Identify the blood parasite species.
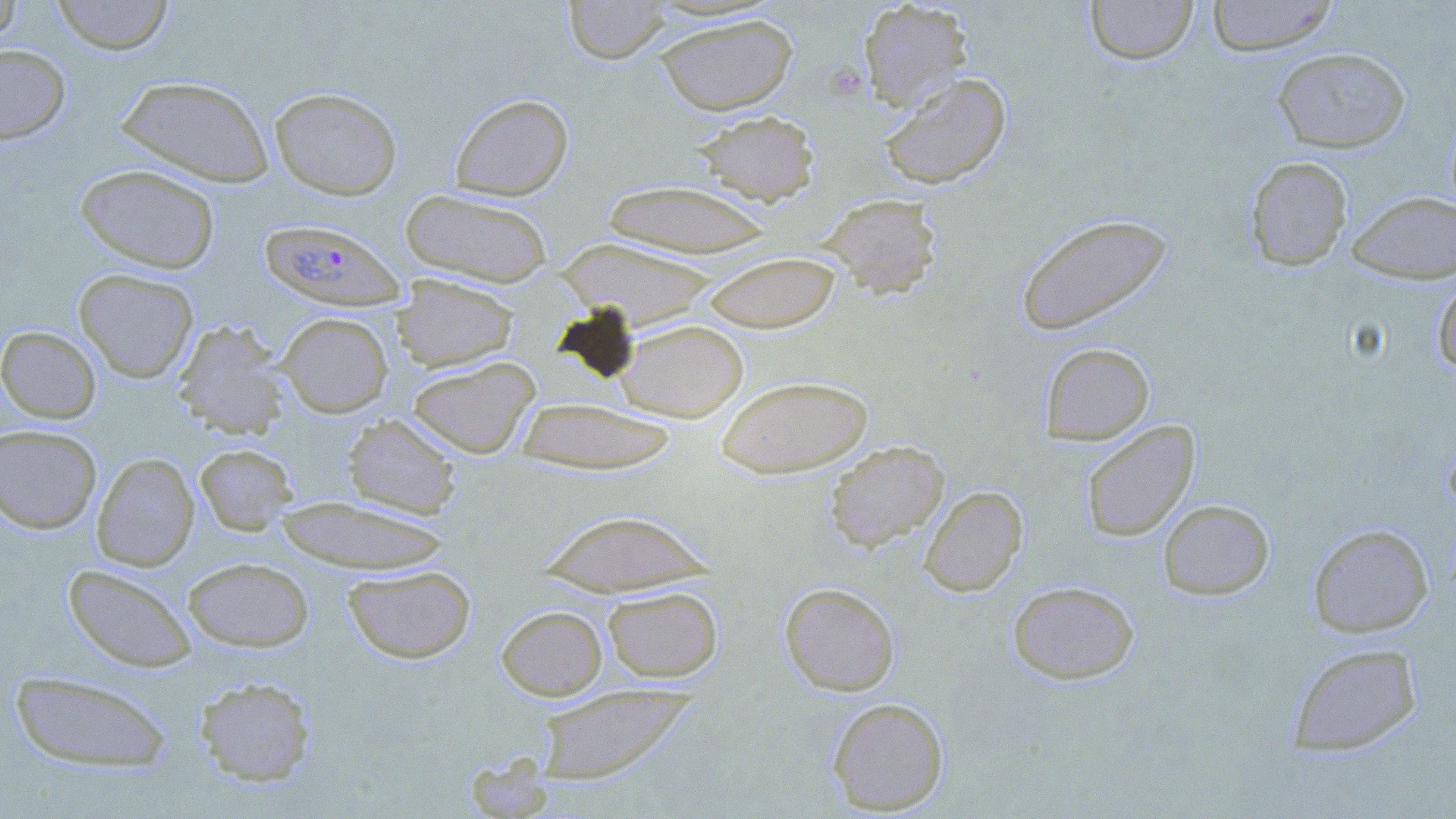

Plasmodium falciparum.

Summary:
  - Coordinate format: approximate bounding boxes as (x1,y1)-(x2,y2) corner pairs in pixels
  - Plasmodium falciparum-infected red blood cell locations: (260,218)-(407,311)
  - Uninfected red blood cell locations: (0,0)-(22,49), (51,0)-(173,56), (564,0)-(672,64), (857,0)-(974,111), (1085,0)-(1198,66), (1205,0)-(1338,57), (653,14)-(798,115), (0,44)-(70,144), (1272,47)-(1411,153), (879,72)-(1012,190), (114,75)-(274,187), (269,87)-(402,200), (449,93)-(573,200), (691,110)-(821,206), (1244,156)-(1352,271), (75,164)-(221,274), (601,180)-(775,258), (400,189)-(554,287), (1346,191)-(1456,283), (818,193)-(943,298), (1015,212)-(1174,337), (555,237)-(720,330), (701,252)-(841,333), (73,268)-(199,382), (391,274)-(519,372), (1433,274)-(1456,376), (277,312)-(393,417), (172,319)-(291,438), (616,319)-(748,422), (0,325)-(102,423), (1040,342)-(1155,445), (407,356)-(541,459), (715,375)-(874,479), (514,398)-(681,474), (342,414)-(462,519), (1080,420)-(1200,542), (0,424)-(101,534), (824,440)-(949,552), (195,443)-(298,535), (91,452)-(199,571), (919,485)-(1028,597), (272,496)-(453,573), (1157,499)-(1274,600), (535,508)-(719,597), (1308,523)-(1433,637), (183,556)-(315,652), (63,563)-(197,673), (343,565)-(477,664), (1007,580)-(1139,684), (780,582)-(900,696), (602,585)-(723,683), (496,605)-(607,700), (1286,642)-(1422,757), (9,670)-(173,772), (194,675)-(317,786), (534,684)-(696,785), (827,697)-(949,815), (465,753)-(554,819)
  - Field of view: single
  - Stain: May-Grünwald-Giemsa
  - Modality: light microscopy
  - Preparation: thin blood film
  - Magnification: 1000x
  - Image size: 1456×819 pixels